Classify this cell by malaria status.
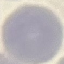
Uninfected.

Summary:
  - Capture: smartphone through the microscope eyepiece
  - Preparation: thin smear
  - Stain: Giemsa
  - Image type: automatically extracted cell patch, resized to 64 × 64 pixels